Classify this cell by malaria status.
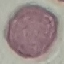

Uninfected.

Giemsa stain. Acquired by smartphone through the microscope eyepiece. Thin smear of blood. Automatically extracted cell patch, resized to 64 × 64 pixels.